Identify the blood parasite species.
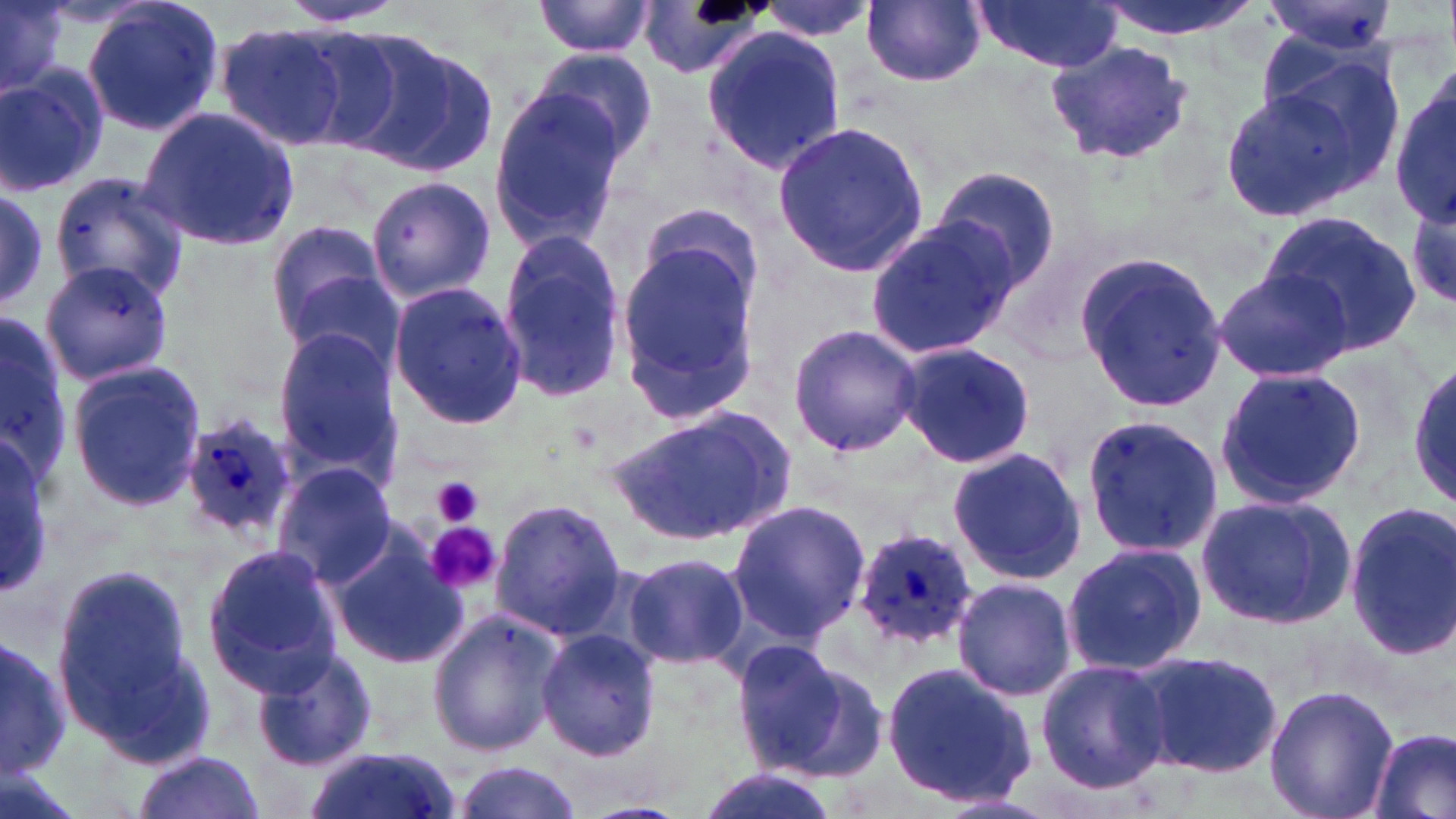

Plasmodium ovale.

Summary:
  - Coordinate format: approximate bounding boxes as named x1/y1/x2/y2 corners in pixels
  - Plasmodium ovale-infected red blood cell locations: (x1=182, y1=410, x2=299, y2=541), (x1=852, y1=527, x2=979, y2=651)
  - Uninfected red blood cell locations: (x1=1, y1=0, x2=65, y2=98), (x1=79, y1=0, x2=225, y2=140), (x1=274, y1=0, x2=416, y2=29), (x1=534, y1=0, x2=656, y2=57), (x1=753, y1=0, x2=878, y2=43), (x1=862, y1=0, x2=988, y2=87), (x1=970, y1=0, x2=1123, y2=73), (x1=1093, y1=0, x2=1261, y2=41), (x1=1262, y1=0, x2=1400, y2=57), (x1=638, y1=4, x2=772, y2=81), (x1=215, y1=21, x2=352, y2=151), (x1=288, y1=22, x2=432, y2=153), (x1=700, y1=27, x2=846, y2=175), (x1=349, y1=34, x2=499, y2=174), (x1=1044, y1=38, x2=1197, y2=166), (x1=1263, y1=44, x2=1406, y2=183), (x1=532, y1=47, x2=659, y2=165), (x1=0, y1=66, x2=110, y2=196), (x1=1391, y1=82, x2=1453, y2=230), (x1=1216, y1=84, x2=1374, y2=225), (x1=488, y1=85, x2=628, y2=253), (x1=139, y1=107, x2=302, y2=252), (x1=772, y1=120, x2=929, y2=275), (x1=931, y1=167, x2=1060, y2=290), (x1=47, y1=168, x2=192, y2=307), (x1=366, y1=175, x2=496, y2=302), (x1=0, y1=188, x2=51, y2=308), (x1=1406, y1=190, x2=1455, y2=313), (x1=1259, y1=212, x2=1423, y2=355), (x1=865, y1=216, x2=1023, y2=359), (x1=263, y1=219, x2=393, y2=344), (x1=615, y1=229, x2=764, y2=425), (x1=493, y1=232, x2=627, y2=403), (x1=1076, y1=252, x2=1226, y2=416), (x1=38, y1=259, x2=174, y2=388), (x1=1212, y1=268, x2=1352, y2=383), (x1=278, y1=272, x2=399, y2=373), (x1=388, y1=283, x2=526, y2=432), (x1=0, y1=315, x2=71, y2=485), (x1=787, y1=321, x2=922, y2=459), (x1=271, y1=327, x2=401, y2=472), (x1=895, y1=344, x2=1036, y2=468), (x1=67, y1=361, x2=207, y2=511), (x1=1409, y1=364, x2=1455, y2=506), (x1=1213, y1=367, x2=1365, y2=509), (x1=606, y1=403, x2=798, y2=548), (x1=1080, y1=411, x2=1224, y2=562), (x1=0, y1=435, x2=54, y2=591), (x1=948, y1=447, x2=1091, y2=586), (x1=270, y1=463, x2=396, y2=588), (x1=1196, y1=493, x2=1357, y2=631), (x1=727, y1=497, x2=870, y2=643), (x1=489, y1=499, x2=625, y2=639), (x1=1343, y1=503, x2=1456, y2=661), (x1=324, y1=528, x2=468, y2=673), (x1=1059, y1=542, x2=1206, y2=679), (x1=202, y1=544, x2=343, y2=695), (x1=623, y1=550, x2=750, y2=671), (x1=50, y1=561, x2=213, y2=765), (x1=951, y1=576, x2=1076, y2=701), (x1=427, y1=609, x2=565, y2=758), (x1=537, y1=630, x2=662, y2=760), (x1=0, y1=635, x2=70, y2=785), (x1=731, y1=641, x2=885, y2=779), (x1=253, y1=646, x2=379, y2=772), (x1=1134, y1=649, x2=1285, y2=780), (x1=1034, y1=659, x2=1172, y2=795), (x1=880, y1=661, x2=1037, y2=808), (x1=1264, y1=685, x2=1396, y2=819), (x1=1368, y1=726, x2=1455, y2=819), (x1=301, y1=748, x2=461, y2=819), (x1=131, y1=751, x2=266, y2=819), (x1=0, y1=758, x2=84, y2=819), (x1=450, y1=761, x2=584, y2=818), (x1=694, y1=768, x2=841, y2=819)
  - Platelet locations: (x1=431, y1=476, x2=485, y2=530), (x1=426, y1=523, x2=503, y2=596)
  - Image size: 1456×819 pixels
  - Field of view: single
  - Modality: optical microscopy
  - Magnification: 1000x
  - Stain: May-Grünwald-Giemsa
  - Preparation: thin blood smear